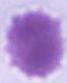

Summary:
  - Modality: photomicrograph
  - Magnification: 1000x
  - Identification: erythrocyte